Locate every Plasmodium parasite.
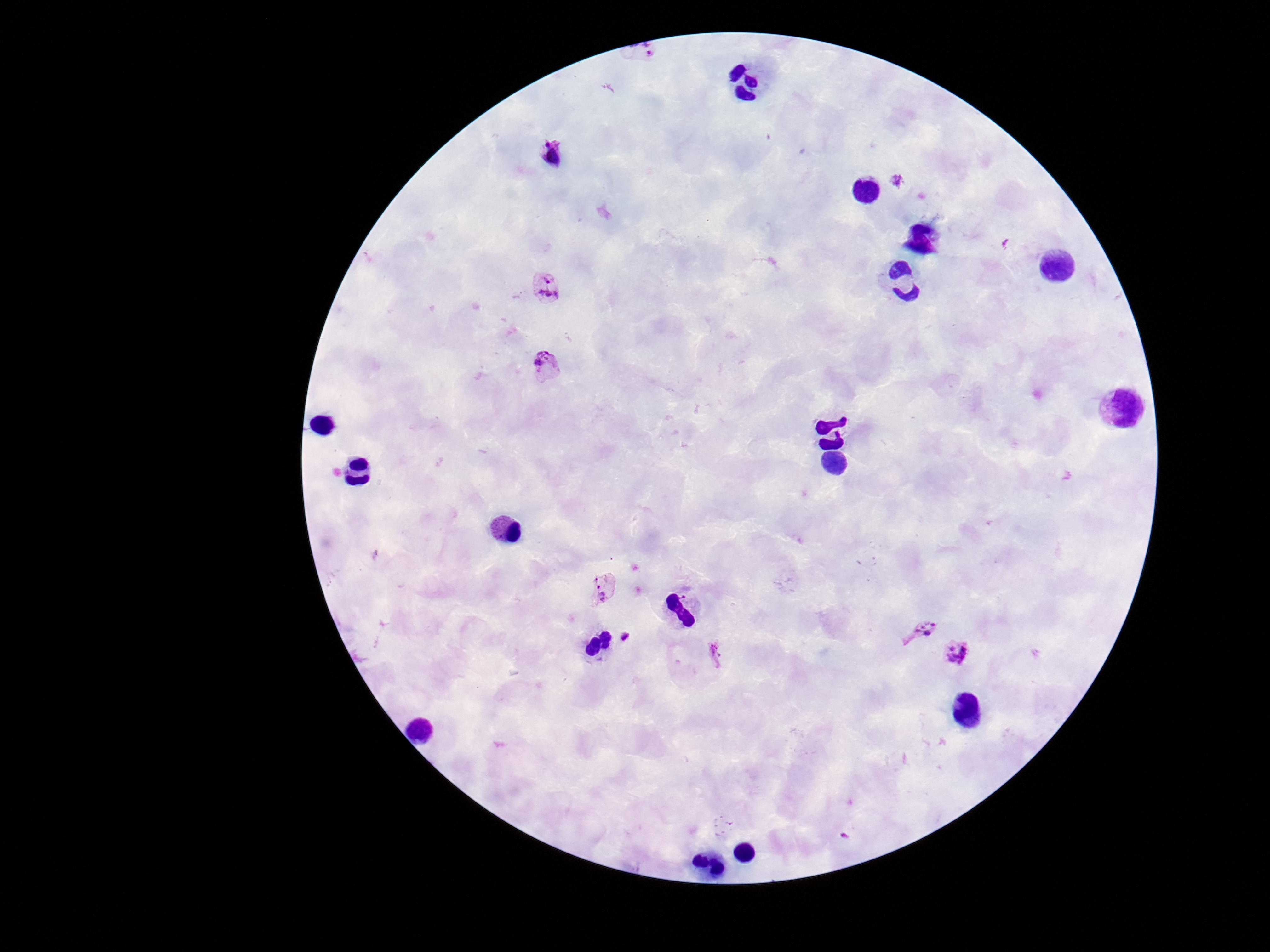
Approximate object centers, in pixels from the top-left corner.
Plasmodium parasites: (x=553, y=156), (x=547, y=286), (x=547, y=366), (x=602, y=589), (x=920, y=629), (x=626, y=636), (x=957, y=654), (x=716, y=655).

Summary:
  - Magnification: 100x
  - Capture: smartphone camera through the microscope eyepiece
  - Field of view: single
  - Preparation: thick peripheral-blood smear
  - Patient malaria status: infected
  - Image size: 1270×952 pixels
  - Stain: Giemsa